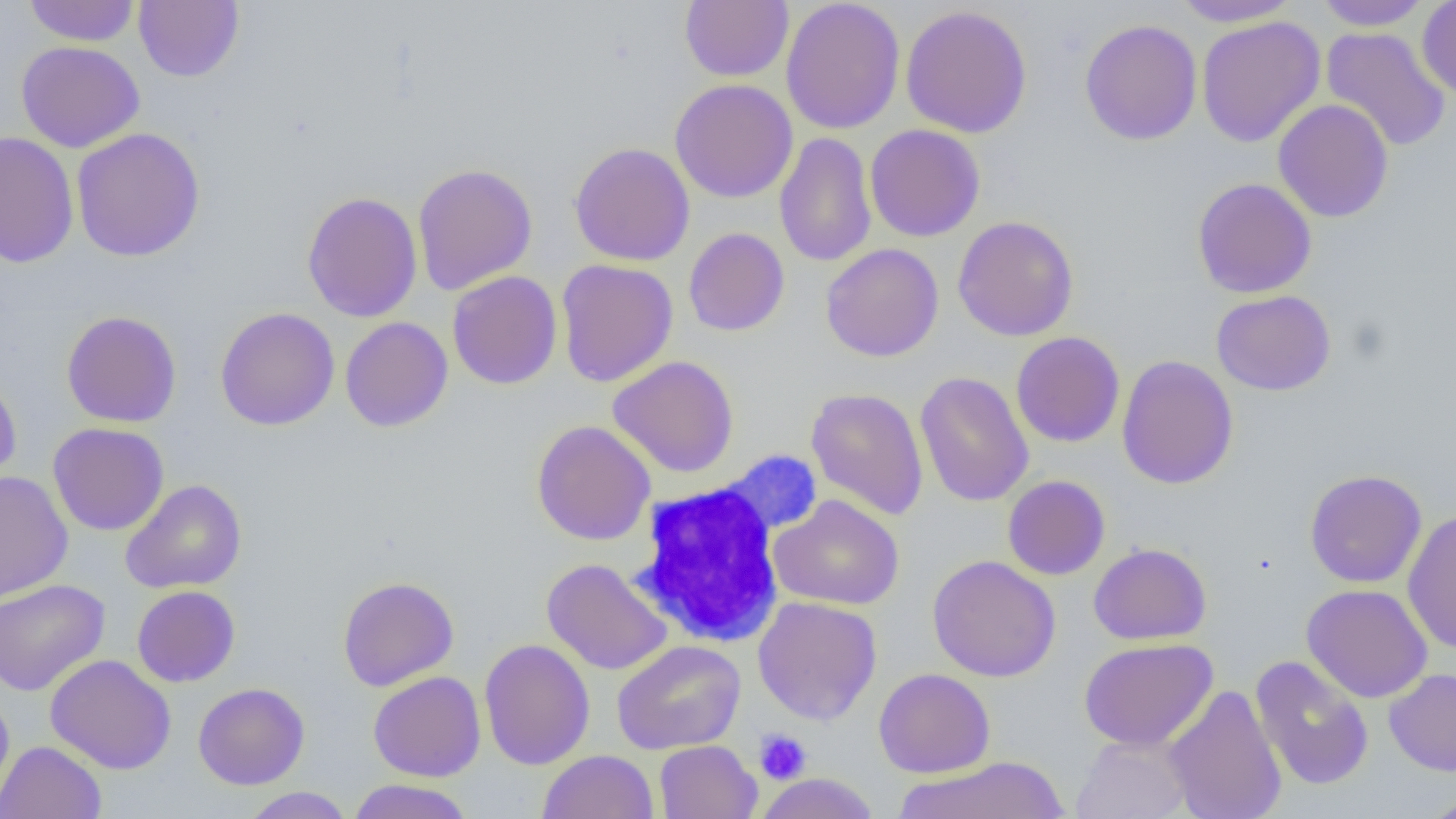
Approximate bounding boxes as named x1/y1/x2/y2 corners in pixels. White blood cell locations: (x1=625, y1=470, x2=803, y2=650). Uninfected red blood cell locations: (x1=24, y1=0, x2=140, y2=46), (x1=134, y1=0, x2=244, y2=82), (x1=680, y1=0, x2=794, y2=82), (x1=781, y1=0, x2=906, y2=135), (x1=1169, y1=0, x2=1303, y2=27), (x1=1314, y1=1, x2=1431, y2=30), (x1=1417, y1=1, x2=1456, y2=100), (x1=900, y1=4, x2=1033, y2=138), (x1=1196, y1=16, x2=1325, y2=147), (x1=1079, y1=18, x2=1202, y2=145), (x1=1321, y1=27, x2=1451, y2=152), (x1=16, y1=41, x2=145, y2=152), (x1=670, y1=78, x2=798, y2=203), (x1=1273, y1=99, x2=1394, y2=223), (x1=864, y1=124, x2=985, y2=242), (x1=71, y1=127, x2=205, y2=262), (x1=1, y1=132, x2=78, y2=268), (x1=774, y1=132, x2=878, y2=267), (x1=569, y1=142, x2=696, y2=266), (x1=412, y1=163, x2=538, y2=295), (x1=1192, y1=177, x2=1317, y2=298), (x1=302, y1=191, x2=422, y2=322), (x1=952, y1=216, x2=1079, y2=341), (x1=683, y1=227, x2=790, y2=336), (x1=820, y1=243, x2=944, y2=362), (x1=556, y1=259, x2=678, y2=387), (x1=447, y1=270, x2=562, y2=389), (x1=1211, y1=290, x2=1336, y2=396), (x1=215, y1=307, x2=339, y2=431), (x1=62, y1=311, x2=182, y2=427), (x1=340, y1=316, x2=453, y2=432), (x1=1011, y1=332, x2=1125, y2=447), (x1=1116, y1=354, x2=1239, y2=490), (x1=607, y1=356, x2=739, y2=478), (x1=915, y1=370, x2=1034, y2=507), (x1=0, y1=371, x2=22, y2=487), (x1=806, y1=388, x2=929, y2=520), (x1=532, y1=420, x2=656, y2=545), (x1=48, y1=422, x2=169, y2=535), (x1=1304, y1=469, x2=1427, y2=588), (x1=0, y1=470, x2=73, y2=602), (x1=1003, y1=475, x2=1110, y2=580), (x1=120, y1=479, x2=247, y2=594), (x1=768, y1=494, x2=905, y2=610), (x1=1402, y1=509, x2=1456, y2=655), (x1=1088, y1=542, x2=1212, y2=645), (x1=927, y1=555, x2=1061, y2=682), (x1=541, y1=558, x2=672, y2=676), (x1=338, y1=575, x2=459, y2=691), (x1=0, y1=578, x2=111, y2=696), (x1=1301, y1=583, x2=1433, y2=703), (x1=131, y1=585, x2=240, y2=687), (x1=753, y1=596, x2=882, y2=725), (x1=478, y1=638, x2=595, y2=770), (x1=1078, y1=638, x2=1218, y2=751), (x1=611, y1=640, x2=746, y2=755), (x1=45, y1=654, x2=176, y2=774), (x1=1250, y1=655, x2=1374, y2=791), (x1=873, y1=668, x2=995, y2=778), (x1=1384, y1=668, x2=1456, y2=776), (x1=368, y1=671, x2=486, y2=782), (x1=193, y1=682, x2=309, y2=790), (x1=1163, y1=684, x2=1287, y2=819), (x1=0, y1=691, x2=14, y2=807), (x1=1071, y1=733, x2=1195, y2=819), (x1=654, y1=740, x2=761, y2=818), (x1=0, y1=741, x2=106, y2=819), (x1=538, y1=750, x2=658, y2=819), (x1=892, y1=755, x2=1070, y2=819), (x1=756, y1=773, x2=878, y2=819), (x1=347, y1=779, x2=475, y2=819), (x1=240, y1=787, x2=353, y2=818), (x1=1419, y1=792, x2=1456, y2=819). Platelet locations: (x1=754, y1=729, x2=812, y2=785). Slide-level diagnosis: no evidence of blood parasites. Thin blood film. Image is 1456×819 pixels. Captured at 1000x magnification. Optical microscopy. One field of a larger specimen.